Classify this cell by malaria status.
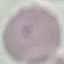

It is uninfected.

Photographed with a smartphone camera at the microscope eyepiece. Thin blood smear. Automatically extracted cell patch, resized to 64 × 64 pixels. Giemsa-stained preparation.